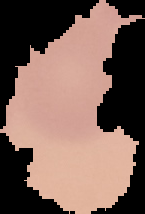 Segmented cell region on a black background. From a thin blood film. Image is 145×214 pixels. Malaria status: uninfected.